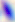
Summary:
  - Modality: photomicrograph
  - Identification: Toxoplasma gondii
  - Magnification: 400x